Locate Plasmodium parasites and leukocytes.
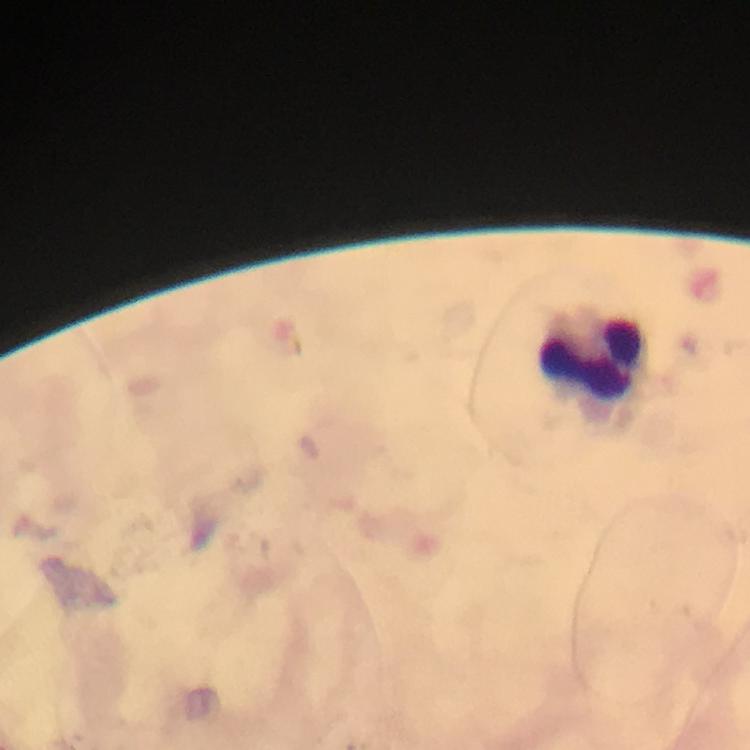
No Plasmodium parasites detected.
Approximate centers as [x, y] in pixels.
Leukocytes: [593, 363].

Summary:
  - Preparation: thick smear
  - Capture: smartphone mounted on the microscope
  - Stain: Giemsa
  - Image size: 750×750 pixels
  - Context: from a diagnostic examination for malaria
  - Magnification: 100x
  - Immersion oil: applied
  - Cropped from: a single field of view